Outline each Plasmodium malariae-infected red blood cell.
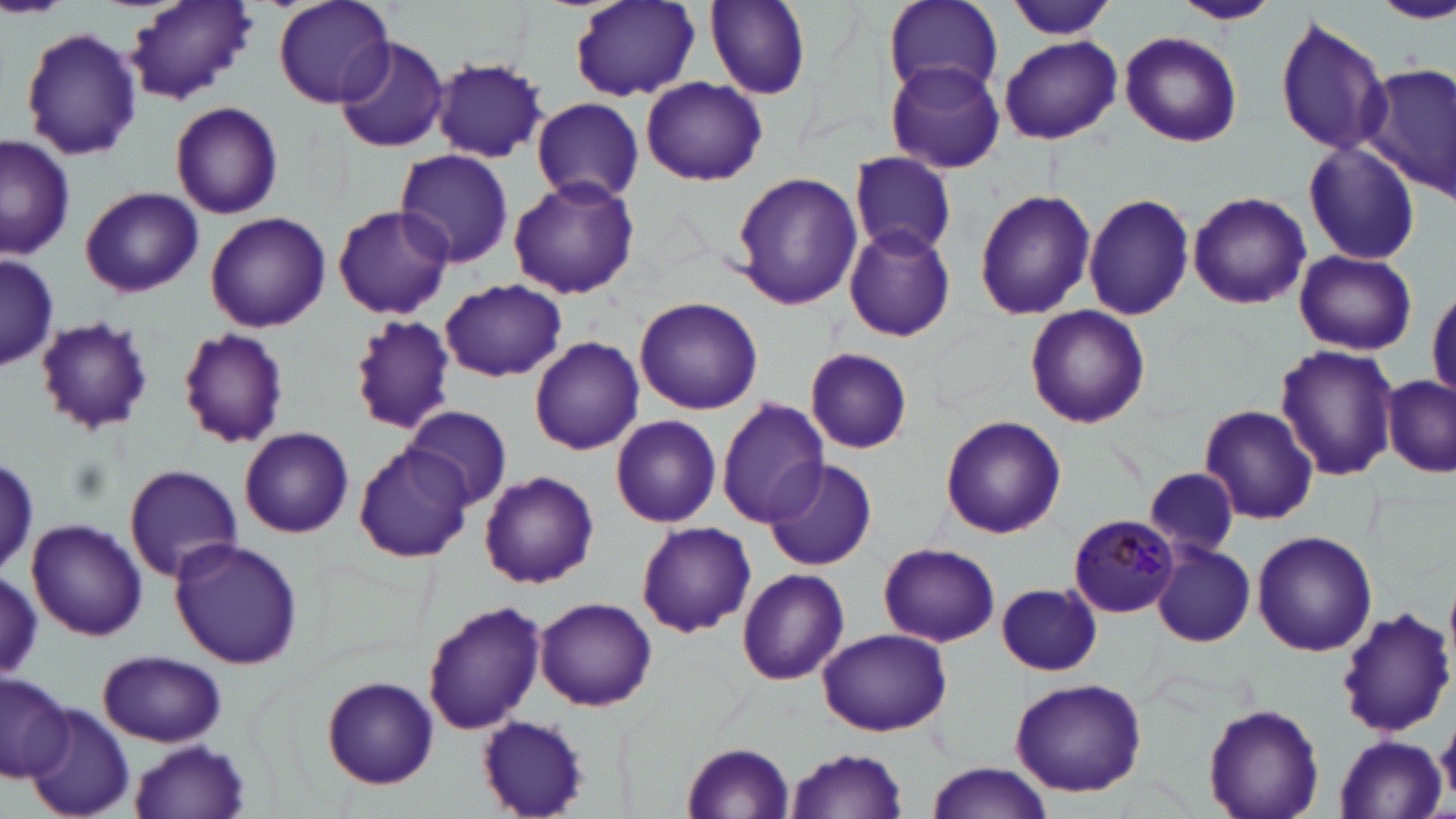

Approximate bounding boxes as named x1/y1/x2/y2 corners in pixels.
Plasmodium malariae-infected red blood cells: (x1=1067, y1=514, x2=1178, y2=618).

slide_level_diagnosis: Plasmodium malariae
stain: May-Grünwald-Giemsa
preparation: thin blood film
uninfected_red_blood_cell_locations: 'approximate bounding boxes as named x1/y1/x2/y2 corners in pixels: (x1=272, y1=0, x2=398, y2=108), (x1=571, y1=0, x2=700, y2=102), (x1=702, y1=0, x2=813, y2=102), (x1=1004, y1=0, x2=1118, y2=42), (x1=1174, y1=0, x2=1279, y2=25), (x1=1376, y1=0, x2=1456, y2=23), (x1=125, y1=1, x2=258, y2=104), (x1=882, y1=1, x2=1005, y2=96), (x1=1275, y1=16, x2=1392, y2=158), (x1=20, y1=26, x2=143, y2=161), (x1=1119, y1=31, x2=1242, y2=147), (x1=333, y1=35, x2=450, y2=153), (x1=999, y1=35, x2=1121, y2=144), (x1=432, y1=60, x2=549, y2=162), (x1=885, y1=61, x2=1006, y2=173), (x1=1362, y1=63, x2=1456, y2=198), (x1=639, y1=76, x2=767, y2=186), (x1=531, y1=97, x2=643, y2=204), (x1=168, y1=100, x2=284, y2=219), (x1=1, y1=135, x2=77, y2=261), (x1=1302, y1=139, x2=1421, y2=266), (x1=396, y1=149, x2=514, y2=268), (x1=850, y1=151, x2=956, y2=258), (x1=730, y1=169, x2=862, y2=310), (x1=506, y1=176, x2=641, y2=300), (x1=80, y1=185, x2=204, y2=297), (x1=973, y1=188, x2=1093, y2=320), (x1=1188, y1=191, x2=1311, y2=310), (x1=1082, y1=192, x2=1195, y2=321), (x1=332, y1=205, x2=453, y2=319), (x1=203, y1=211, x2=330, y2=331), (x1=842, y1=224, x2=957, y2=342), (x1=1293, y1=249, x2=1417, y2=355), (x1=0, y1=255, x2=60, y2=372), (x1=440, y1=279, x2=566, y2=381), (x1=1428, y1=287, x2=1456, y2=398), (x1=635, y1=296, x2=763, y2=414), (x1=1023, y1=304, x2=1150, y2=429), (x1=350, y1=313, x2=457, y2=435), (x1=35, y1=317, x2=153, y2=434), (x1=176, y1=326, x2=290, y2=449), (x1=530, y1=337, x2=645, y2=456), (x1=1276, y1=344, x2=1399, y2=481), (x1=802, y1=347, x2=913, y2=452), (x1=1381, y1=375, x2=1455, y2=477), (x1=715, y1=397, x2=831, y2=527), (x1=405, y1=405, x2=512, y2=509), (x1=1199, y1=405, x2=1320, y2=525), (x1=611, y1=414, x2=722, y2=528), (x1=941, y1=415, x2=1066, y2=538), (x1=239, y1=427, x2=354, y2=539), (x1=352, y1=444, x2=475, y2=562), (x1=0, y1=452, x2=38, y2=578), (x1=765, y1=460, x2=877, y2=571), (x1=122, y1=464, x2=245, y2=582), (x1=1145, y1=466, x2=1241, y2=558), (x1=479, y1=470, x2=599, y2=589), (x1=25, y1=518, x2=147, y2=642), (x1=637, y1=522, x2=756, y2=637), (x1=1253, y1=531, x2=1378, y2=656), (x1=168, y1=537, x2=302, y2=670), (x1=878, y1=541, x2=999, y2=646), (x1=1152, y1=543, x2=1255, y2=647), (x1=736, y1=569, x2=849, y2=686), (x1=0, y1=570, x2=45, y2=679), (x1=995, y1=583, x2=1101, y2=676), (x1=535, y1=597, x2=656, y2=712), (x1=422, y1=601, x2=545, y2=735), (x1=1333, y1=605, x2=1455, y2=738), (x1=815, y1=627, x2=952, y2=736), (x1=98, y1=651, x2=227, y2=747), (x1=0, y1=671, x2=73, y2=782), (x1=321, y1=676, x2=439, y2=789), (x1=1010, y1=678, x2=1148, y2=796), (x1=1204, y1=702, x2=1325, y2=819), (x1=24, y1=706, x2=135, y2=818), (x1=475, y1=715, x2=590, y2=819), (x1=1437, y1=716, x2=1456, y2=804), (x1=1332, y1=732, x2=1446, y2=819), (x1=129, y1=741, x2=251, y2=817), (x1=681, y1=741, x2=795, y2=817), (x1=785, y1=749, x2=911, y2=817), (x1=927, y1=761, x2=1055, y2=816)'
field_of_view: single
magnification: 1000x
image_size: 1456×819 pixels
modality: light microscopy